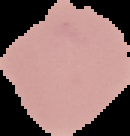 From a thin blood smear. Result: no Plasmodium parasites seen. Image is 130×136 pixels. The area outside the segmented cell region is set to black.